Report the malaria status of this cell.
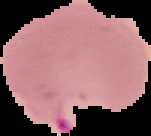

It is parasitized.

{
  "image_type": "segmented cell region on a black background",
  "image_size": "151×136 pixels",
  "preparation": "thin blood smear"
}